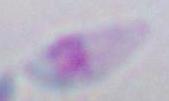
Photomicrograph. Toxoplasma gondii is shown. 1000x magnification.